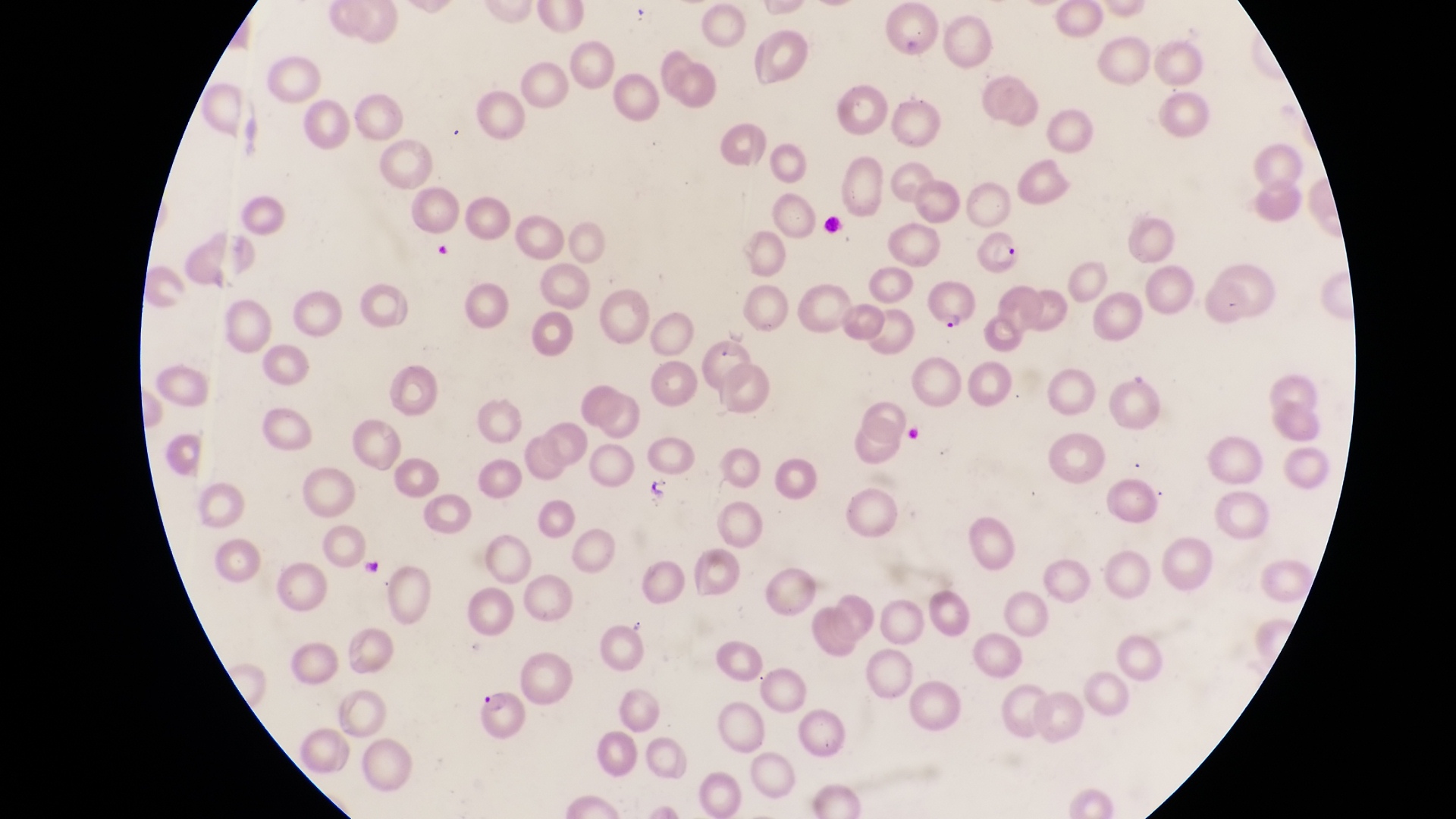
Approximate bounding boxes as left top right bottom in pixels. Artifact (platelet-like body, stain precipitate, or debris) locations: 644 475 678 504; 354 554 386 583. Parasitised red blood cell locations: 973 237 1023 279; 924 284 980 337; 466 687 527 742. One field of view. Magnification of 1000x. Photographed through the eyepiece of an Olympus CX-23 microscope with a smartphone camera. Thin blood smear. Image is 1456×819 pixels. Collected in Uganda.